Look for Plasmodium parasites.
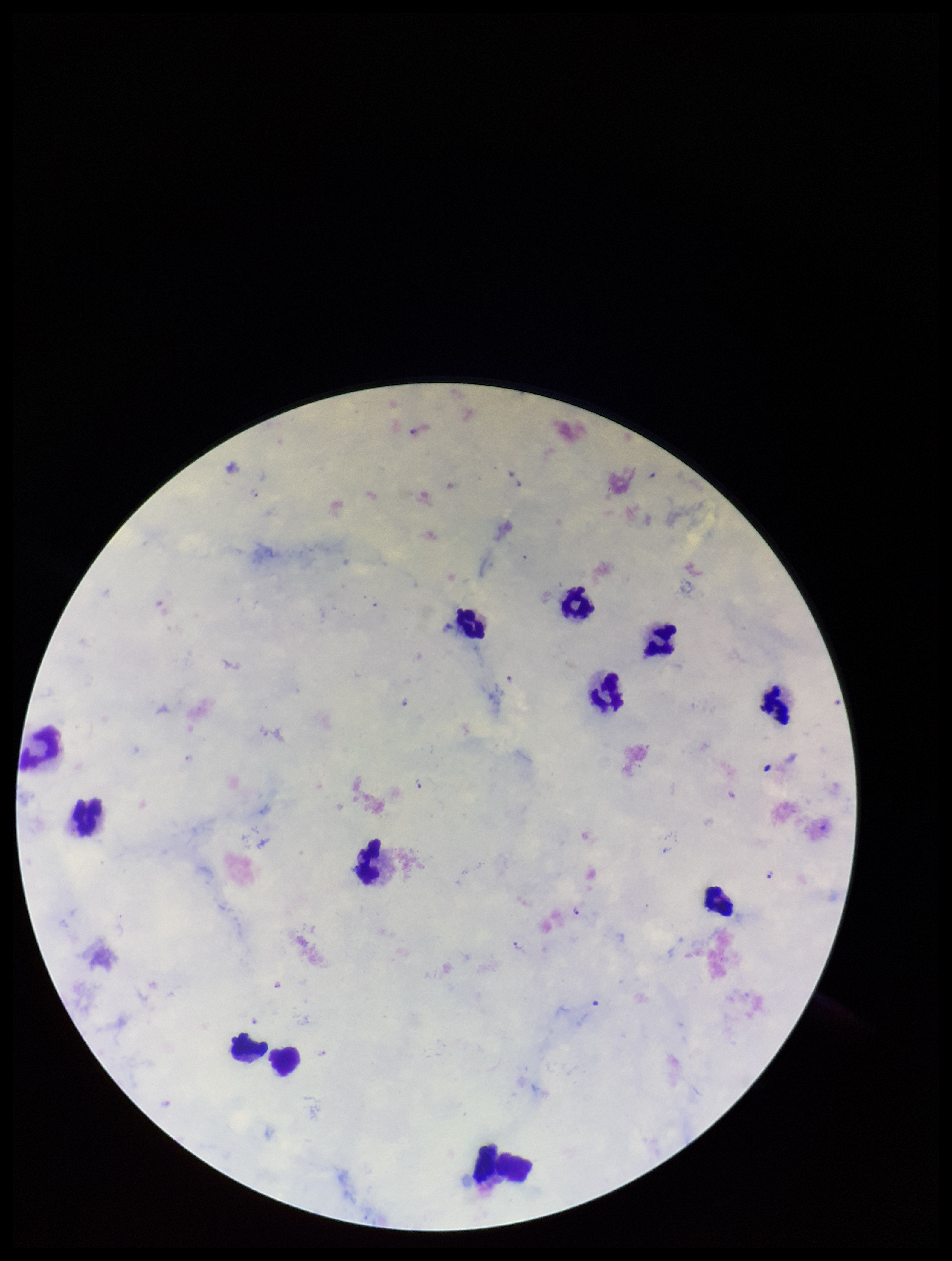
Identified.

Giemsa stain. Preparation: thick smear. Single field of view. Species reported for this patient: Plasmodium falciparum. Image is 952×1261 pixels. Smartphone photograph taken through the eyepiece of a microscope. Parasite count: 6. Leukocyte count: 12. Patient malaria status: positive.